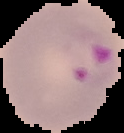

Summary:
  - Image type: segmented cell region on a black background
  - Preparation: thin blood film
  - Result: malaria parasites identified
  - Image size: 124×133 pixels